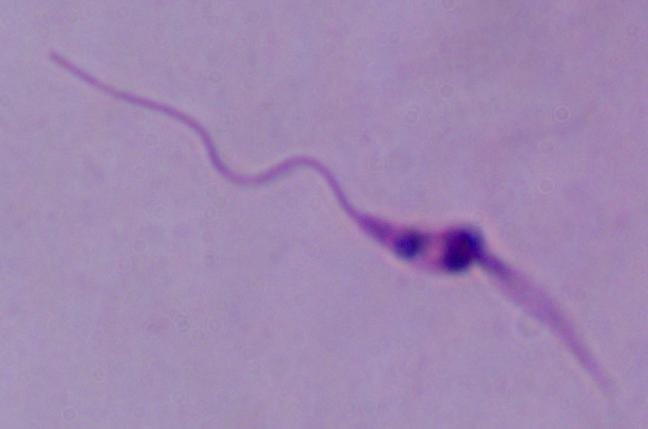
1000x magnification. A Leishmania parasite is shown. Photomicrograph.